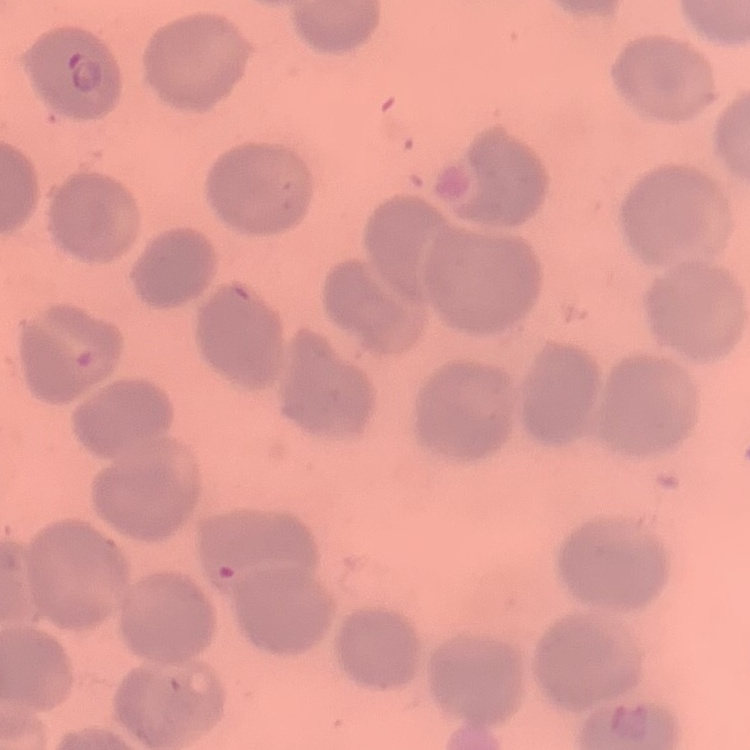
The erythrocytes show no rouleaux formation. Thin blood film. One tile cut from a larger photomicrograph. Field's or Giemsa stain.